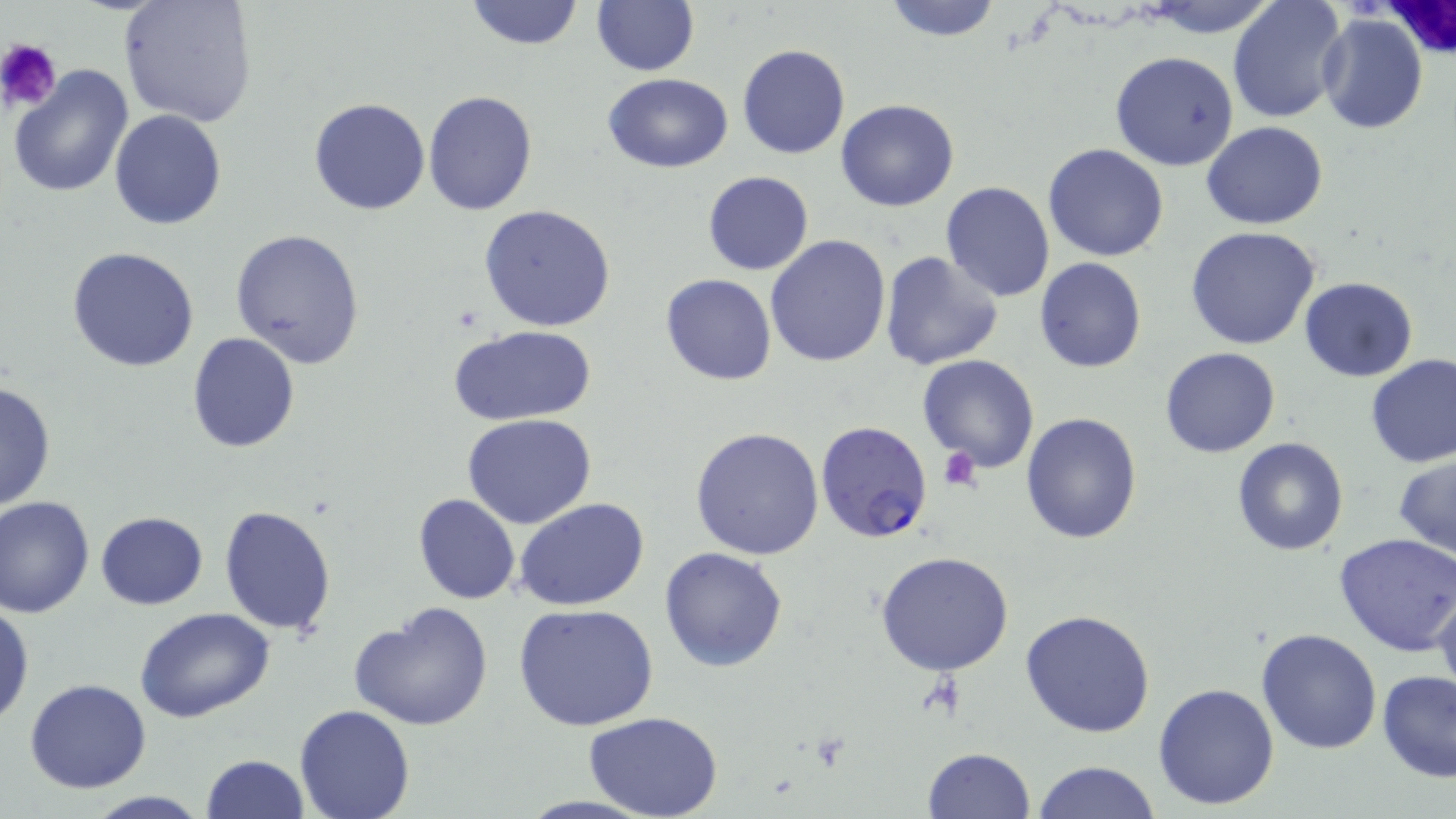

Summary:
  - Coordinate format: approximate bounding boxes as (x1,y1)-(x2,y2) corner pairs in pixels
  - Uninfected red blood cell locations: (117,0)-(259,127), (464,0)-(584,50), (591,0)-(700,76), (881,0)-(1005,42), (1142,1)-(1281,35), (1228,1)-(1348,123), (1316,13)-(1430,134), (737,43)-(851,160), (1109,50)-(1239,170), (8,64)-(134,197), (603,73)-(732,173), (423,89)-(538,214), (309,98)-(431,216), (836,99)-(959,213), (109,110)-(227,229), (1203,121)-(1328,230), (1043,143)-(1168,261), (702,171)-(814,275), (939,182)-(1056,301), (478,203)-(618,333), (230,226)-(366,369), (1186,227)-(1322,351), (765,235)-(892,369), (68,245)-(200,372), (878,251)-(1005,371), (1034,257)-(1146,373), (661,272)-(777,386), (1299,276)-(1418,381), (449,324)-(597,426), (187,332)-(300,454), (1159,347)-(1282,459), (917,355)-(1041,474), (1366,355)-(1456,469), (0,379)-(56,513), (1021,412)-(1142,544), (464,413)-(598,530), (690,426)-(826,561), (1231,436)-(1349,556), (1393,452)-(1456,561), (412,492)-(520,605), (0,495)-(95,617), (514,495)-(650,612), (219,504)-(337,634), (96,511)-(208,609), (1333,533)-(1456,657), (659,547)-(788,671), (876,552)-(1017,677), (1433,577)-(1456,699), (0,598)-(35,728), (348,601)-(493,731), (514,603)-(660,732), (133,607)-(276,724), (1019,608)-(1156,738), (1256,627)-(1381,754), (1376,669)-(1456,782), (24,679)-(151,793), (1152,682)-(1281,811), (294,703)-(416,819), (584,713)-(725,819), (921,748)-(1035,819), (201,755)-(308,819), (1033,760)-(1160,818), (77,790)-(216,819)
  - White blood cell locations: (1374,2)-(1456,63)
  - Plasmodium falciparum-infected red blood cell locations: (816,420)-(934,542)
  - Platelet locations: (1,39)-(61,110), (937,448)-(980,490)
  - Slide-level diagnosis: Plasmodium falciparum
  - Image size: 1456×819 pixels
  - Magnification: 1000x
  - Stain: May-Grünwald-Giemsa
  - Preparation: thin blood film
  - Field of view: single
  - Modality: optical microscopy